Report the malaria status of this cell.
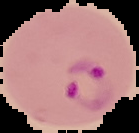

It is parasitized.

Image is 139×133 pixels. Cell region segmented out of the field of view; the surrounding area is masked to black. From a thin blood film.